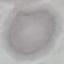

malaria status = uninfected
stain = Giemsa
preparation = thin smear
capture = smartphone camera at the microscope eyepiece
image type = cell patch, automatically extracted from a larger field of view and resized to 64 × 64 pixels